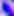

Toxoplasma gondii is seen. Photomicrograph. 400x magnification.